Outline each Plasmodium falciparum-infected red blood cell.
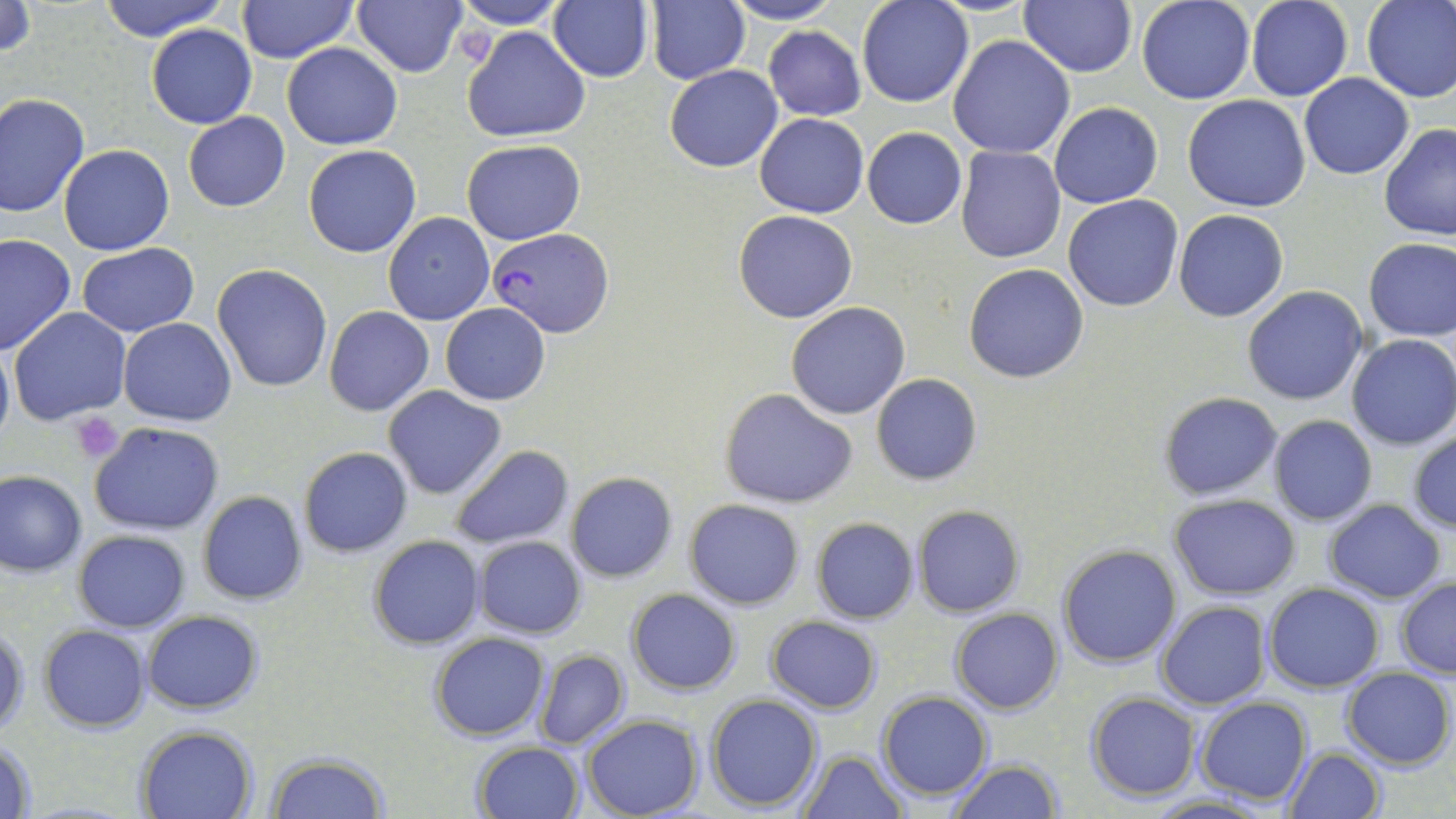

Approximate bounding boxes as [x1, y1, x2, y2] in pixels.
Plasmodium falciparum-infected red blood cells: [487, 226, 614, 338].

slide-level diagnosis = Plasmodium falciparum
platelet locations = approximate bounding boxes as [x1, y1, x2, y2] in pixels: [71, 411, 125, 462]
preparation = thin blood smear
image size = 1456×819 pixels
stain = May-Grünwald-Giemsa
modality = optical microscopy
field of view = single
uninfected red blood cell locations = approximate bounding boxes as [x1, y1, x2, y2] in pixels: [98, 0, 229, 42], [237, 0, 356, 65], [353, 0, 466, 77], [647, 0, 750, 86], [722, 0, 845, 25], [858, 0, 973, 107], [1018, 0, 1138, 76], [1136, 0, 1255, 104], [1362, 0, 1456, 102], [452, 1, 569, 29], [548, 1, 653, 83], [1244, 1, 1352, 102], [1, 2, 36, 60], [147, 23, 256, 129], [464, 25, 590, 142], [763, 26, 866, 120], [948, 35, 1075, 158], [281, 42, 401, 149], [665, 65, 783, 172], [1298, 73, 1413, 180], [0, 93, 90, 217], [1183, 94, 1312, 212], [1049, 102, 1162, 208], [183, 111, 290, 212], [755, 112, 869, 217], [1378, 124, 1456, 241], [862, 127, 968, 229], [462, 140, 586, 245], [58, 144, 175, 256], [302, 145, 421, 258], [955, 148, 1067, 263], [1063, 194, 1183, 312], [1174, 209, 1289, 323], [734, 210, 857, 323], [384, 212, 495, 325], [0, 234, 75, 356], [1364, 237, 1456, 342], [76, 243, 199, 337], [211, 264, 334, 392], [964, 264, 1089, 383], [1242, 285, 1369, 406], [440, 302, 549, 406], [786, 302, 910, 419], [8, 306, 130, 425], [324, 306, 433, 415], [119, 318, 236, 425], [1347, 334, 1456, 450], [0, 337, 13, 452], [872, 373, 982, 486], [384, 386, 507, 498], [720, 388, 857, 508], [1158, 391, 1284, 500], [1269, 414, 1378, 525], [89, 422, 224, 534], [1407, 429, 1456, 535], [449, 444, 574, 550], [299, 446, 413, 557], [0, 472, 86, 577], [566, 472, 676, 582], [198, 492, 307, 605], [1169, 495, 1299, 599], [684, 499, 805, 609], [1323, 499, 1446, 603], [912, 504, 1024, 616], [811, 518, 918, 624], [73, 529, 191, 632], [369, 534, 484, 650], [473, 536, 588, 638], [1059, 544, 1182, 666], [1396, 578, 1456, 678], [1264, 582, 1384, 692], [626, 589, 742, 694], [1156, 600, 1271, 710], [951, 608, 1062, 714], [142, 610, 262, 712], [766, 615, 881, 713], [0, 625, 28, 737], [40, 625, 151, 732], [430, 632, 551, 741], [533, 648, 629, 750], [1342, 666, 1455, 771], [877, 691, 993, 801], [1086, 693, 1199, 800], [705, 694, 822, 811], [1195, 697, 1311, 805], [581, 715, 703, 819], [135, 725, 258, 818], [1, 738, 39, 818], [472, 742, 584, 819], [1283, 746, 1384, 818], [797, 749, 906, 819], [267, 753, 388, 819], [948, 761, 1064, 818], [1145, 793, 1279, 818]
magnification = 1000x